Give a bounding box for every leukocyte visible.
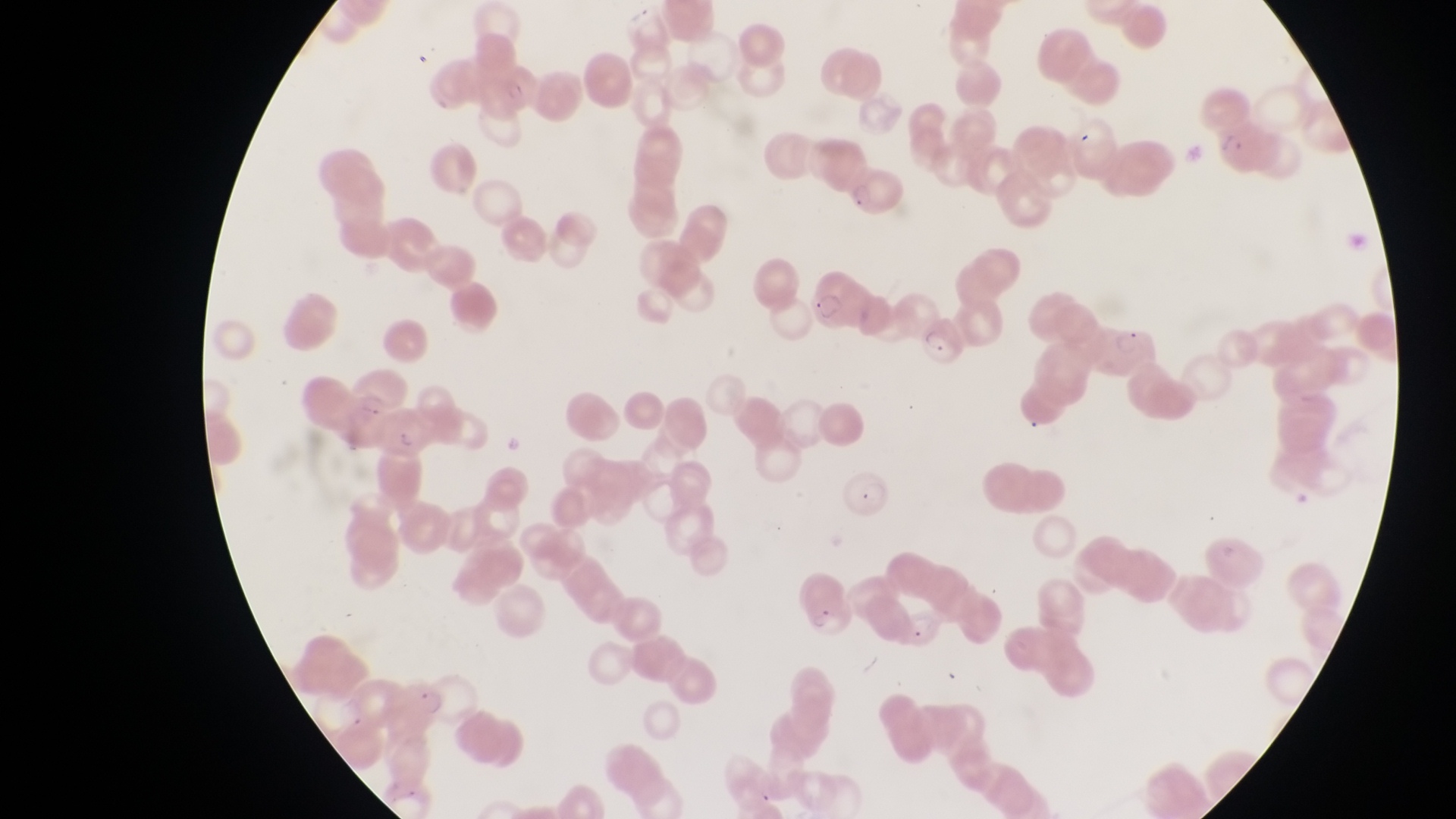

No leukocytes observed.

{
  "preparation": "thin blood film",
  "image_size": "1456×819 pixels",
  "magnification": "1000x",
  "field_of_view": "single",
  "capture": "smartphone photograph through the eyepiece of an Olympus CX-23 microscope",
  "country": "Uganda",
  "parasitised_red_blood_cell_locations": "approximate bounding boxes as (left, top, right, bottom) in pixels: (489, 63, 542, 119), (1208, 115, 1281, 179), (842, 164, 903, 220), (808, 271, 866, 340), (912, 310, 967, 373), (1097, 317, 1160, 378), (369, 409, 427, 462), (838, 472, 893, 519), (793, 571, 845, 629), (400, 679, 450, 719)"
}